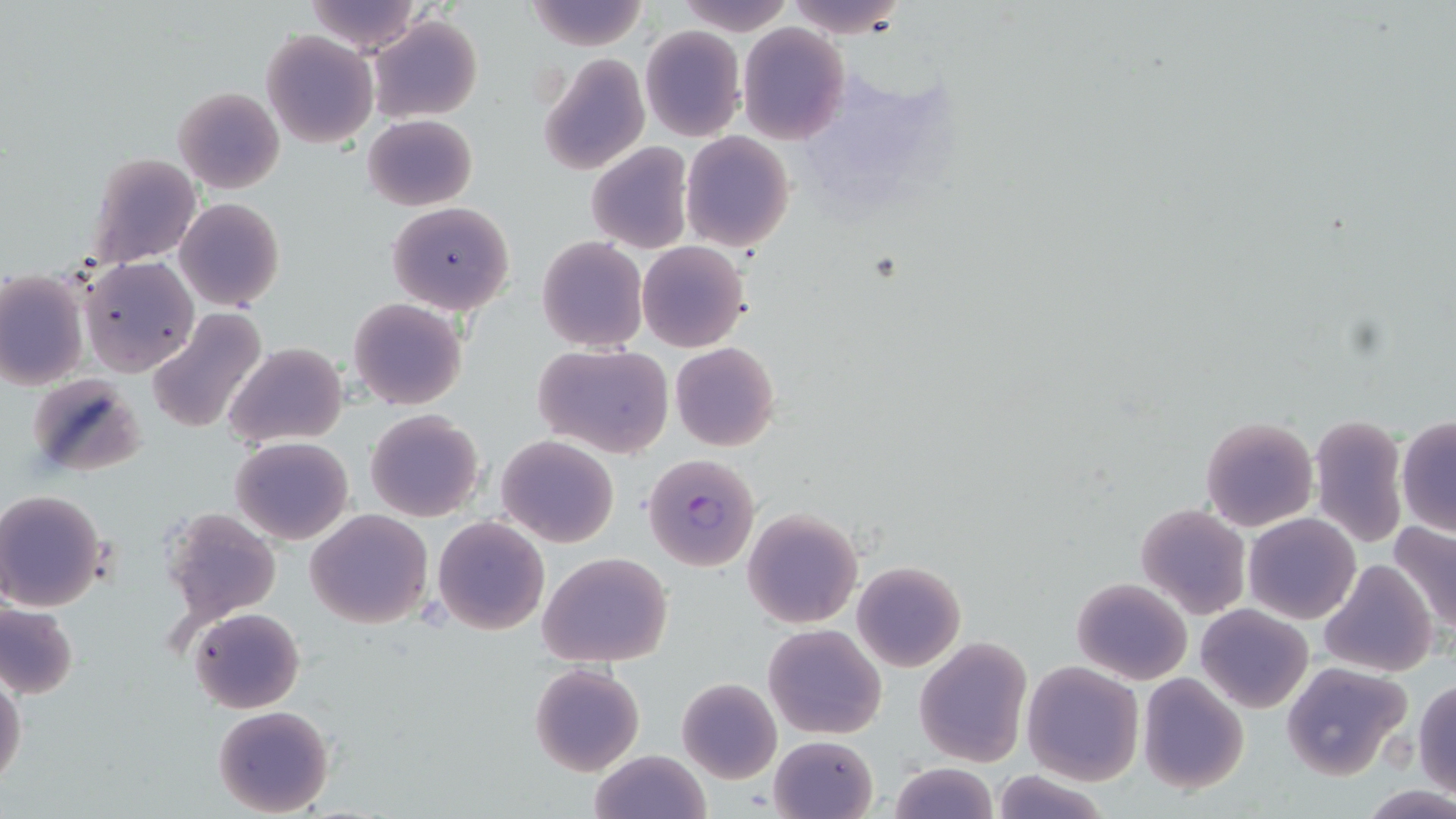
slide_level_diagnosis: Plasmodium falciparum
field_of_view: one of a larger specimen
modality: light microscopy
uninfected_red_blood_cell_locations: 'approximate bounding boxes as (x1, y1, x2, y2) in pixels: (303, 0, 422, 53), (526, 0, 648, 51), (681, 0, 794, 34), (788, 0, 907, 36), (367, 15, 482, 122), (738, 24, 851, 146), (640, 27, 746, 141), (263, 30, 376, 148), (540, 54, 650, 175), (172, 86, 285, 193), (363, 114, 477, 211), (680, 131, 796, 254), (587, 142, 693, 254), (82, 152, 202, 271), (176, 197, 284, 311), (387, 201, 515, 314), (537, 236, 647, 352), (637, 241, 750, 353), (79, 257, 197, 375), (1, 273, 87, 390), (348, 298, 467, 410), (146, 309, 268, 434), (670, 341, 779, 452), (224, 342, 348, 448), (533, 344, 675, 460), (26, 375, 143, 478), (365, 409, 485, 523), (1308, 413, 1407, 550), (1201, 416, 1318, 532), (1396, 417, 1456, 537), (497, 435, 618, 547), (231, 436, 354, 545), (0, 488, 109, 611), (1136, 504, 1251, 619), (161, 505, 283, 627), (742, 507, 864, 629), (305, 509, 433, 629), (1243, 512, 1359, 623), (432, 517, 550, 636), (1389, 519, 1456, 633), (538, 552, 673, 667), (1321, 559, 1436, 677), (852, 560, 965, 672), (1072, 576, 1191, 685), (0, 602, 78, 698), (1196, 604, 1313, 713), (190, 607, 305, 713), (763, 623, 887, 739), (915, 637, 1032, 767), (529, 662, 645, 776), (1023, 662, 1145, 784), (1281, 663, 1412, 780), (0, 671, 26, 791), (1137, 672, 1249, 794), (677, 677, 782, 784), (1414, 679, 1456, 798), (213, 705, 335, 817), (771, 735, 878, 818), (588, 750, 710, 819), (889, 763, 997, 819), (991, 767, 1112, 819)'
preparation: thin blood film
magnification: 1000x
plasmodium_falciparum_infected_red_blood_cell_locations: 'approximate bounding boxes as (x1, y1, x2, y2) in pixels: (642, 453, 760, 572)'
stain: May-Grünwald-Giemsa
image_size: 1456×819 pixels